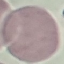

{
  "result": "no malaria parasites detected",
  "preparation": "thin blood film",
  "capture": "smartphone camera at the microscope eyepiece",
  "stain": "Giemsa",
  "image_type": "cell patch, automatically extracted from a larger field of view and resized to 64 × 64 pixels"
}